Report the malaria status of this cell.
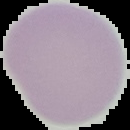

Uninfected.

Summary:
  - Image type: cell region segmented out of the field of view; surrounding area masked to black
  - Image size: 130×130 pixels
  - Preparation: thin blood film